Assess this cell for malaria.
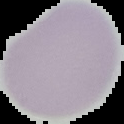
Uninfected.

Image is 124×124 pixels. Segmented cell region on a black background. From a thin blood smear.